Comment on the morphology of the red blood cells.
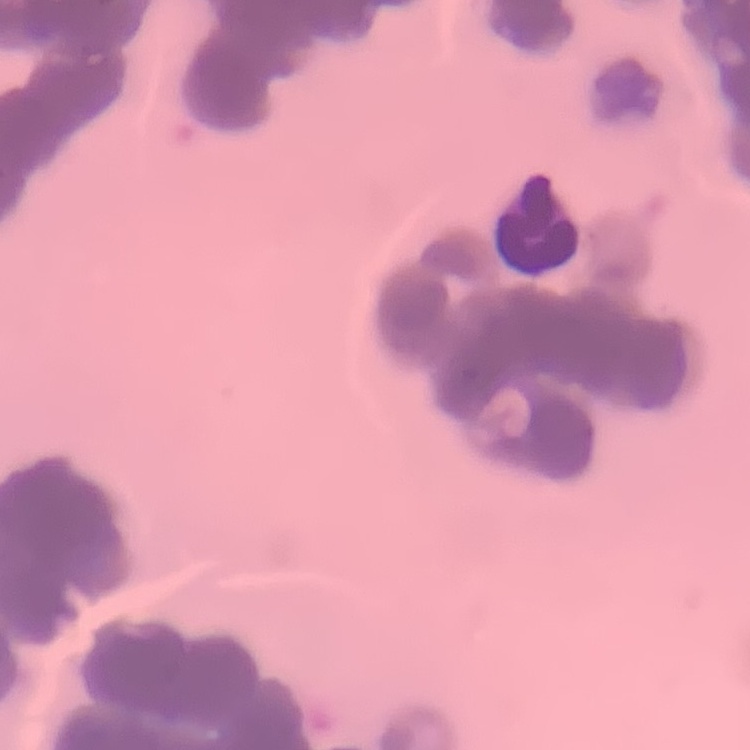

Rouleaux formation.

Stained with either Field's or Giemsa. Square crop of a larger photomicrograph. Thin blood smear.